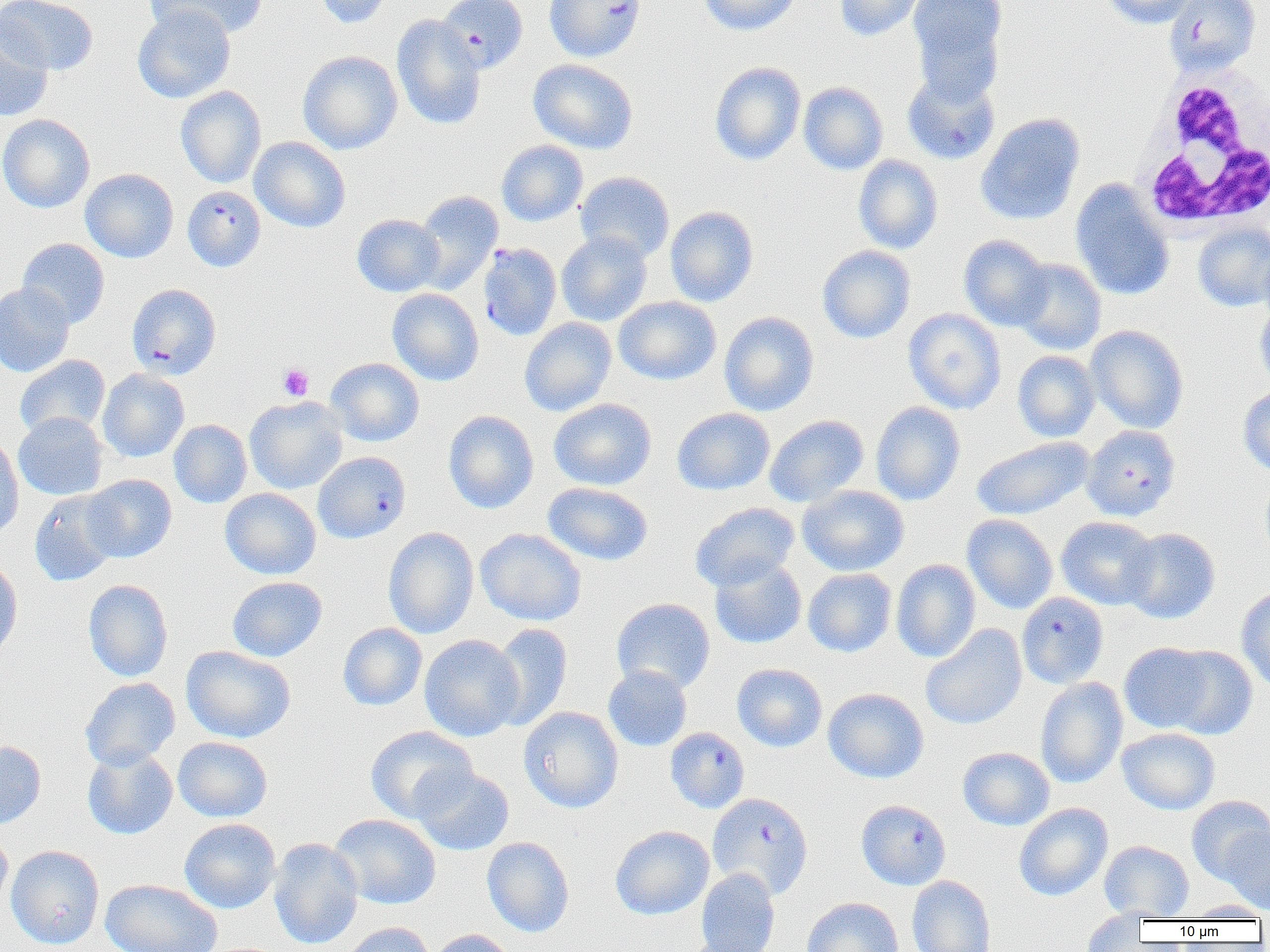

Approximate bounding boxes as named x1/y1/x2/y2 corners in pixels. Plasmodium falciparum-infected red blood cell locations (subset): (x1=437, y1=0, x2=528, y2=74), (x1=544, y1=0, x2=646, y2=62), (x1=1163, y1=0, x2=1260, y2=76), (x1=902, y1=69, x2=1000, y2=165), (x1=183, y1=185, x2=266, y2=271), (x1=478, y1=242, x2=562, y2=341), (x1=127, y1=283, x2=221, y2=379), (x1=1081, y1=424, x2=1180, y2=521), (x1=1016, y1=592, x2=1109, y2=688), (x1=665, y1=727, x2=750, y2=813), (x1=707, y1=793, x2=813, y2=898), (x1=856, y1=799, x2=951, y2=890). Platelet locations: (x1=278, y1=364, x2=314, y2=400). Uninfected red blood cell locations (subset): (x1=1, y1=0, x2=98, y2=76), (x1=145, y1=0, x2=270, y2=41), (x1=313, y1=0, x2=393, y2=29), (x1=697, y1=0, x2=801, y2=36), (x1=835, y1=0, x2=925, y2=41), (x1=908, y1=0, x2=1007, y2=88), (x1=1102, y1=0, x2=1200, y2=28), (x1=133, y1=5, x2=235, y2=103), (x1=391, y1=14, x2=487, y2=130), (x1=0, y1=17, x2=54, y2=121), (x1=297, y1=50, x2=403, y2=154), (x1=528, y1=58, x2=639, y2=154), (x1=709, y1=62, x2=806, y2=165), (x1=798, y1=82, x2=888, y2=174), (x1=176, y1=85, x2=266, y2=188), (x1=975, y1=113, x2=1085, y2=225), (x1=0, y1=114, x2=95, y2=213), (x1=250, y1=137, x2=350, y2=232), (x1=496, y1=140, x2=588, y2=227), (x1=853, y1=155, x2=943, y2=254), (x1=81, y1=168, x2=179, y2=262), (x1=574, y1=171, x2=675, y2=263), (x1=1070, y1=180, x2=1174, y2=301), (x1=413, y1=191, x2=503, y2=294), (x1=665, y1=206, x2=759, y2=307), (x1=352, y1=214, x2=445, y2=297), (x1=1193, y1=222, x2=1270, y2=311), (x1=556, y1=231, x2=652, y2=326), (x1=958, y1=235, x2=1052, y2=331), (x1=17, y1=238, x2=110, y2=328), (x1=1259, y1=242, x2=1270, y2=323), (x1=817, y1=245, x2=916, y2=343), (x1=1013, y1=259, x2=1106, y2=355), (x1=0, y1=282, x2=74, y2=376), (x1=387, y1=288, x2=484, y2=386), (x1=613, y1=296, x2=721, y2=385), (x1=1255, y1=301, x2=1270, y2=390), (x1=903, y1=308, x2=1006, y2=414), (x1=719, y1=311, x2=819, y2=416), (x1=519, y1=317, x2=617, y2=416), (x1=1086, y1=325, x2=1189, y2=433), (x1=1012, y1=351, x2=1100, y2=442), (x1=15, y1=355, x2=110, y2=438), (x1=325, y1=357, x2=424, y2=446), (x1=98, y1=369, x2=189, y2=462), (x1=1238, y1=385, x2=1270, y2=476), (x1=244, y1=396, x2=348, y2=494), (x1=549, y1=398, x2=656, y2=490), (x1=871, y1=401, x2=965, y2=505), (x1=672, y1=407, x2=775, y2=495), (x1=443, y1=410, x2=539, y2=513), (x1=13, y1=412, x2=108, y2=500), (x1=764, y1=414, x2=869, y2=507), (x1=169, y1=419, x2=252, y2=508), (x1=0, y1=435, x2=23, y2=540), (x1=971, y1=436, x2=1093, y2=520), (x1=1260, y1=471, x2=1270, y2=562), (x1=82, y1=474, x2=177, y2=562), (x1=543, y1=482, x2=653, y2=566), (x1=798, y1=485, x2=909, y2=576), (x1=220, y1=487, x2=321, y2=579), (x1=29, y1=491, x2=121, y2=586), (x1=690, y1=502, x2=800, y2=591), (x1=962, y1=514, x2=1058, y2=614), (x1=1056, y1=516, x2=1159, y2=609), (x1=383, y1=526, x2=479, y2=639), (x1=1121, y1=527, x2=1220, y2=624), (x1=475, y1=528, x2=587, y2=626), (x1=709, y1=556, x2=807, y2=649), (x1=0, y1=557, x2=23, y2=662), (x1=892, y1=559, x2=980, y2=662), (x1=803, y1=568, x2=896, y2=657), (x1=227, y1=576, x2=327, y2=662), (x1=83, y1=579, x2=173, y2=681), (x1=1236, y1=584, x2=1270, y2=692), (x1=611, y1=597, x2=715, y2=694), (x1=337, y1=622, x2=427, y2=711), (x1=489, y1=623, x2=573, y2=731), (x1=920, y1=624, x2=1027, y2=729), (x1=419, y1=634, x2=523, y2=741), (x1=1119, y1=643, x2=1214, y2=733), (x1=181, y1=645, x2=295, y2=743), (x1=1163, y1=645, x2=1258, y2=739), (x1=732, y1=663, x2=827, y2=752), (x1=603, y1=664, x2=692, y2=751), (x1=1035, y1=676, x2=1128, y2=788), (x1=80, y1=677, x2=180, y2=770), (x1=823, y1=688, x2=929, y2=783), (x1=518, y1=706, x2=623, y2=813), (x1=365, y1=725, x2=477, y2=822), (x1=1117, y1=727, x2=1220, y2=814), (x1=173, y1=737, x2=272, y2=821), (x1=0, y1=740, x2=46, y2=830), (x1=82, y1=746, x2=177, y2=840), (x1=958, y1=747, x2=1054, y2=830), (x1=412, y1=767, x2=515, y2=855), (x1=1186, y1=795, x2=1270, y2=884), (x1=1013, y1=802, x2=1113, y2=901), (x1=329, y1=813, x2=441, y2=909), (x1=179, y1=818, x2=281, y2=913), (x1=610, y1=825, x2=714, y2=919), (x1=1222, y1=826, x2=1270, y2=915), (x1=0, y1=829, x2=13, y2=916), (x1=482, y1=836, x2=574, y2=937), (x1=268, y1=838, x2=363, y2=949), (x1=1099, y1=840, x2=1194, y2=920), (x1=6, y1=844, x2=104, y2=950), (x1=695, y1=867, x2=780, y2=952), (x1=907, y1=875, x2=996, y2=952), (x1=100, y1=878, x2=223, y2=952), (x1=802, y1=897, x2=903, y2=952), (x1=1184, y1=901, x2=1269, y2=920), (x1=1081, y1=909, x2=1150, y2=951), (x1=340, y1=922, x2=436, y2=952), (x1=428, y1=929, x2=516, y2=952), (x1=675, y1=937, x2=774, y2=952). White blood cell locations: (x1=1132, y1=66, x2=1270, y2=234). Slide-level diagnosis: Plasmodium falciparum. One field of a larger specimen. Image is 1270×952 pixels. Light microscopy. Captured at 1000x magnification. Thin blood film.